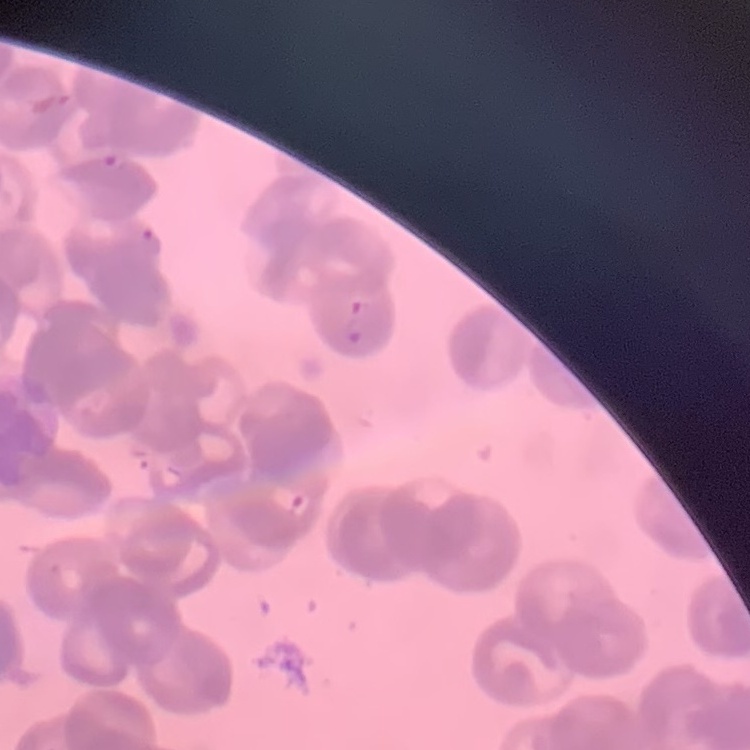
Summary:
  - Red blood cell morphology: rouleaux formation
  - Preparation: thin blood smear
  - Stain: Field's or Giemsa
  - Image type: one tile cut from a larger photomicrograph